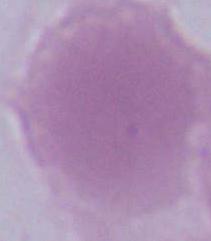
Summary:
  - Magnification: 1000x
  - Modality: micrograph
  - Identification: erythrocyte